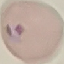

result = no malaria parasites seen
capture = smartphone camera at the microscope eyepiece
stain = Giemsa
image type = automatically extracted cell patch, resized to 64 × 64 pixels
preparation = thin blood film